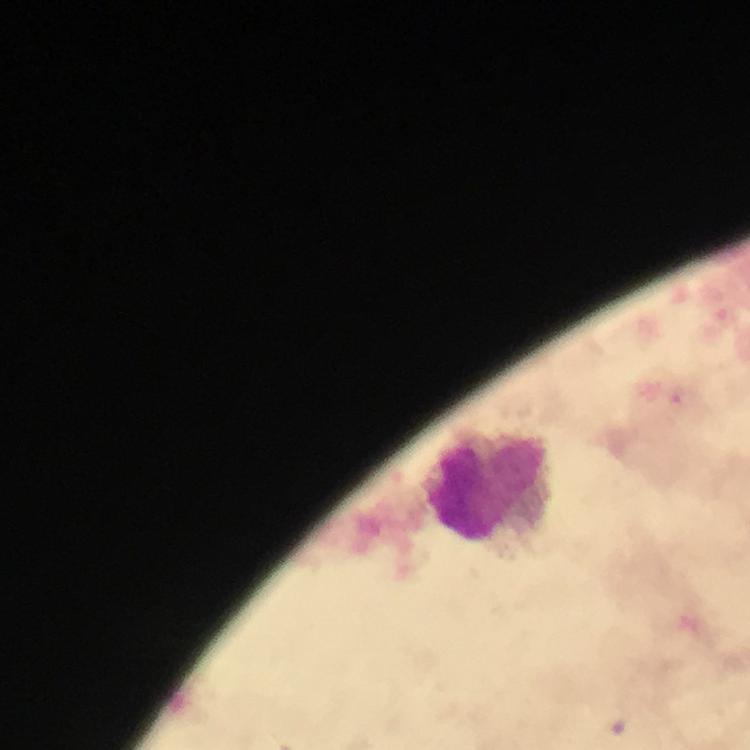 Approximate object centers, in pixels from the top-left corner. Leukocyte locations: (x=486, y=485). Malaria parasite locations: (x=682, y=396). Photographed through the microscope with a smartphone camera. Immersion oil applied. At 100x magnification. A crop from one field of view. From a diagnostic examination for malaria. Thick blood film. Image is 750×750 pixels. Giemsa-stained preparation.